Describe the morphology of the red blood cells.
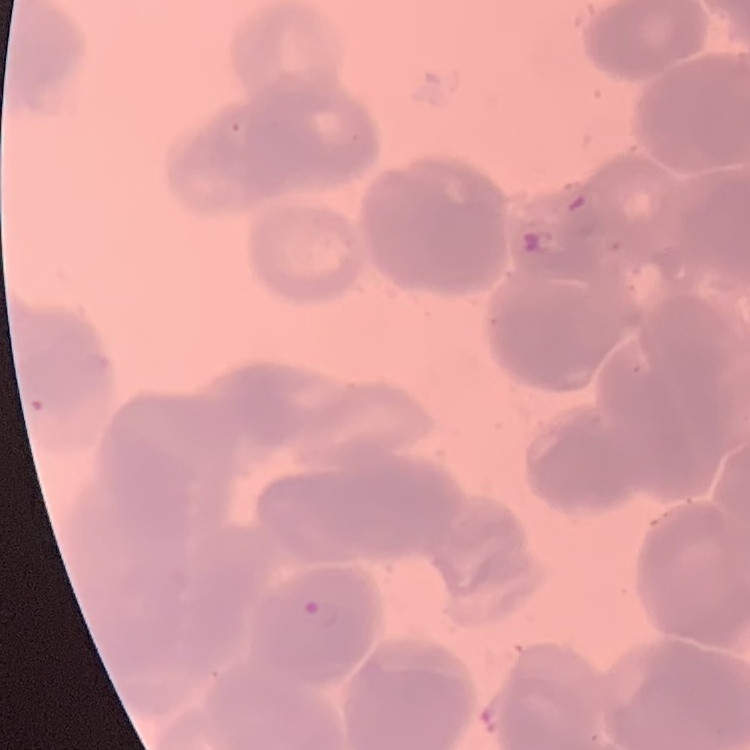
Rouleaux formation.

image type = square crop of a larger photomicrograph
stain = Field's or Giemsa
preparation = thin blood film